Locate and identify every blood parasite.
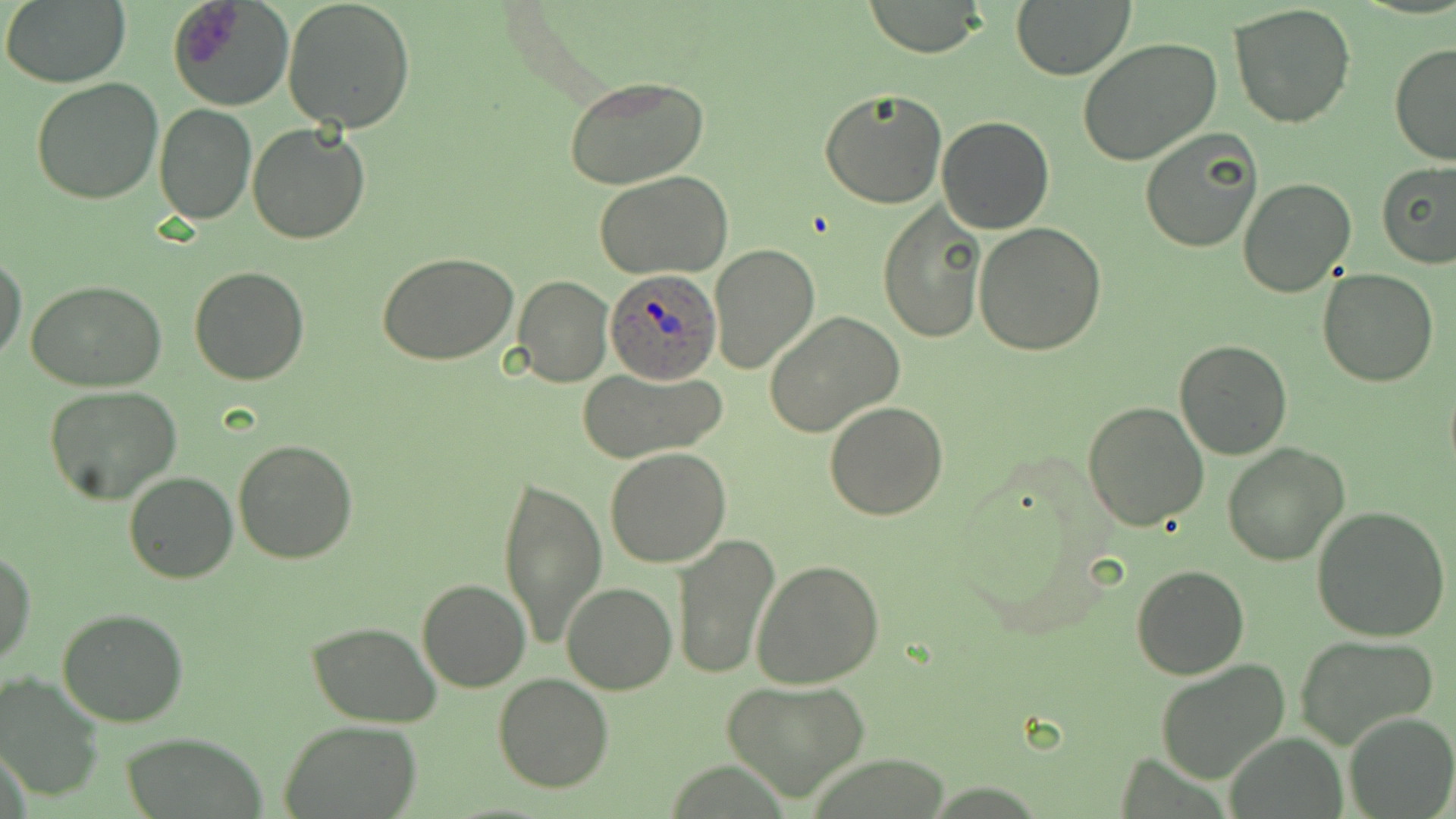

Approximate bounding boxes as named x1/y1/x2/y2 corners in pixels.
Plasmodium ovale-infected red blood cells: (x1=604, y1=267, x2=724, y2=386).
No Plasmodium falciparum, Plasmodium malariae, Plasmodium vivax, Babesia divergens, or Trypanosoma brucei observed.

Summary:
  - Uninfected red blood cell locations: (x1=2, y1=0, x2=130, y2=87), (x1=169, y1=0, x2=293, y2=113), (x1=281, y1=0, x2=417, y2=134), (x1=862, y1=0, x2=989, y2=57), (x1=1011, y1=0, x2=1135, y2=80), (x1=1229, y1=3, x2=1356, y2=129), (x1=1076, y1=37, x2=1222, y2=165), (x1=1389, y1=42, x2=1456, y2=165), (x1=563, y1=73, x2=710, y2=190), (x1=31, y1=78, x2=165, y2=205), (x1=820, y1=87, x2=947, y2=208), (x1=154, y1=103, x2=258, y2=223), (x1=936, y1=116, x2=1054, y2=234), (x1=247, y1=122, x2=372, y2=244), (x1=1139, y1=128, x2=1262, y2=252), (x1=1376, y1=160, x2=1456, y2=269), (x1=595, y1=171, x2=735, y2=278), (x1=1238, y1=176, x2=1358, y2=298), (x1=879, y1=202, x2=987, y2=342), (x1=974, y1=222, x2=1108, y2=356), (x1=708, y1=242, x2=820, y2=377), (x1=0, y1=253, x2=24, y2=365), (x1=378, y1=253, x2=518, y2=366), (x1=189, y1=265, x2=309, y2=385), (x1=1319, y1=268, x2=1437, y2=387), (x1=513, y1=275, x2=615, y2=388), (x1=25, y1=280, x2=168, y2=391), (x1=764, y1=311, x2=904, y2=440), (x1=1173, y1=338, x2=1291, y2=460), (x1=576, y1=368, x2=728, y2=463), (x1=44, y1=385, x2=182, y2=505), (x1=824, y1=400, x2=949, y2=519), (x1=1082, y1=401, x2=1210, y2=531), (x1=233, y1=439, x2=357, y2=564), (x1=1223, y1=443, x2=1350, y2=566), (x1=605, y1=447, x2=730, y2=567), (x1=500, y1=471, x2=606, y2=652), (x1=124, y1=472, x2=237, y2=584), (x1=1311, y1=506, x2=1451, y2=641), (x1=671, y1=531, x2=782, y2=681), (x1=0, y1=547, x2=35, y2=666), (x1=752, y1=559, x2=885, y2=687), (x1=1131, y1=563, x2=1250, y2=680), (x1=417, y1=578, x2=530, y2=692), (x1=561, y1=582, x2=677, y2=695), (x1=57, y1=607, x2=191, y2=728), (x1=306, y1=621, x2=442, y2=728), (x1=1297, y1=634, x2=1439, y2=750), (x1=1154, y1=659, x2=1291, y2=783), (x1=0, y1=670, x2=105, y2=804), (x1=493, y1=671, x2=615, y2=793), (x1=723, y1=678, x2=869, y2=803), (x1=1343, y1=711, x2=1455, y2=819), (x1=280, y1=719, x2=424, y2=818), (x1=118, y1=732, x2=268, y2=819)
  - Slide-level diagnosis: Plasmodium ovale
  - Stain: May-Grünwald-Giemsa
  - Magnification: 1000x
  - Preparation: thin blood smear
  - Field of view: one of a larger specimen
  - Modality: light microscopy
  - Image size: 1456×819 pixels